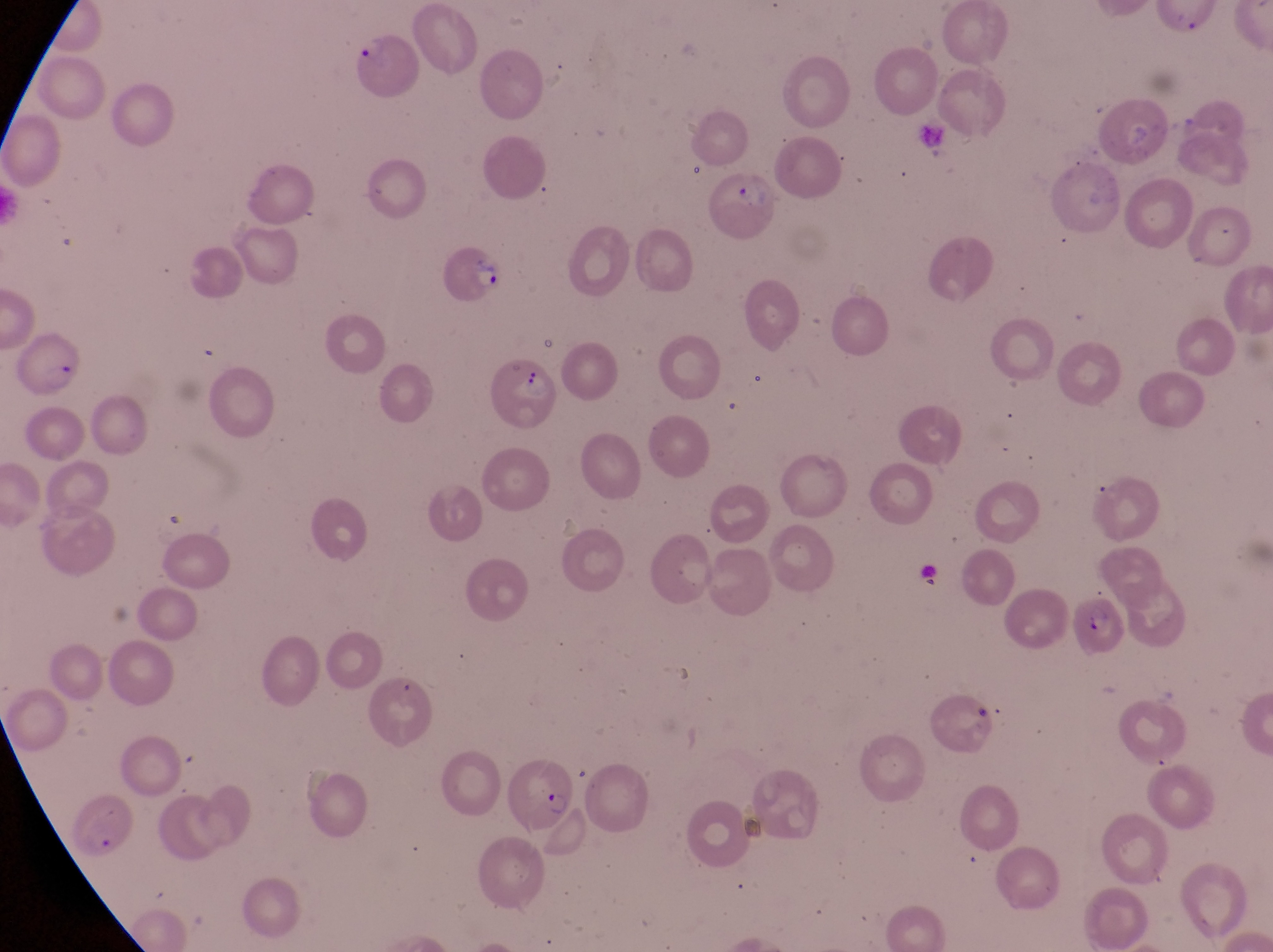

Approximate bounding boxes as {left, top, right, bottom} in pixels.
Summary:
  - Parasitised red blood cell locations: {347, 30, 427, 100}, {702, 162, 780, 240}, {439, 235, 504, 310}, {15, 335, 84, 398}, {484, 352, 558, 432}, {1064, 594, 1131, 656}, {495, 767, 572, 829}
  - Object labeled both artifact (platelet-like body, stain precipitate, or debris) and trophozoite by the source: {914, 556, 953, 599}
  - Image size: 1273×952 pixels
  - Country: Uganda
  - Field of view: single
  - Capture: smartphone photograph through the eyepiece of an Olympus CX-23 microscope
  - Preparation: thin blood smear
  - Magnification: 1000x